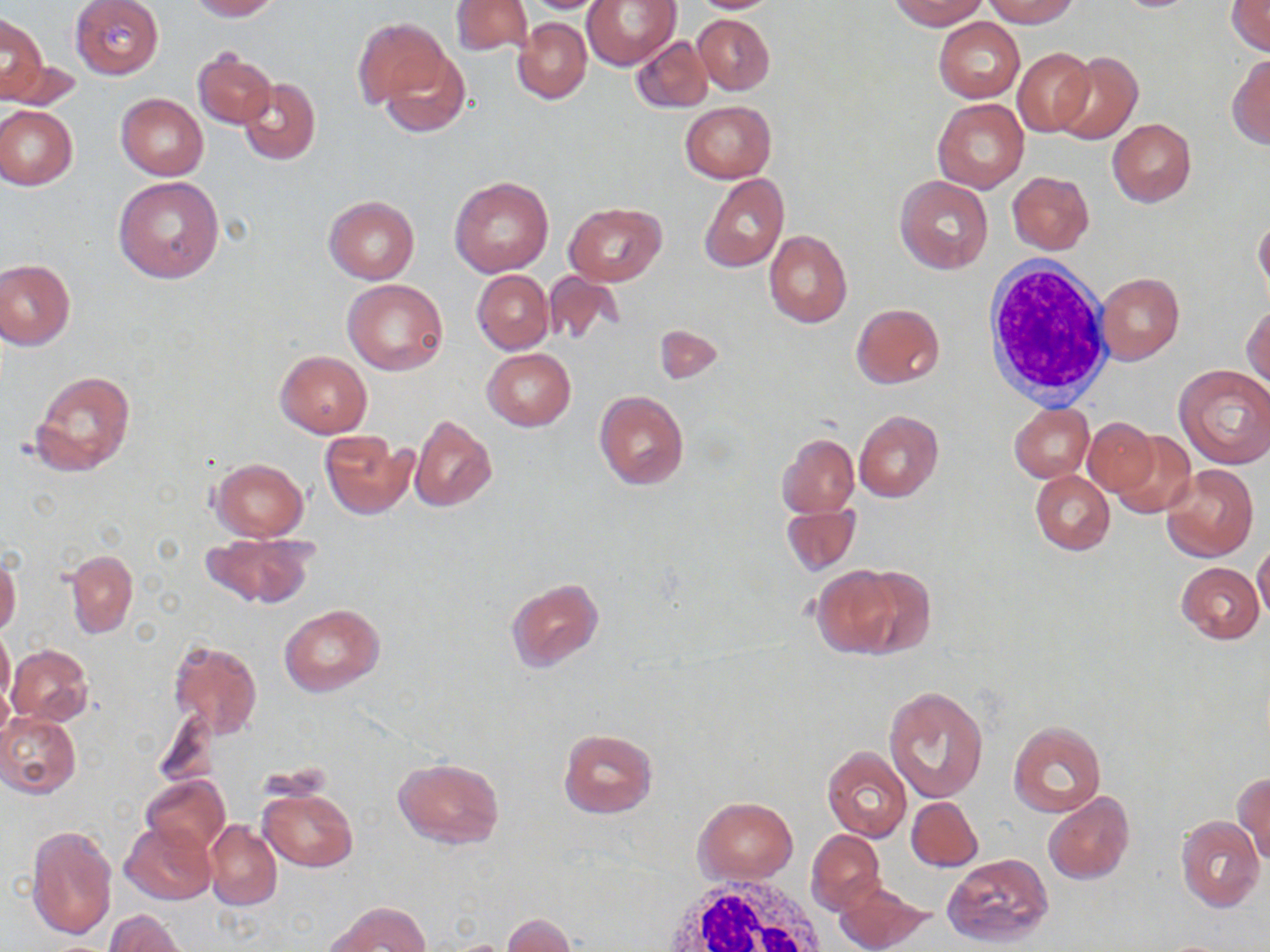
slide-level diagnosis = negative for blood parasites
white blood cell locations = approximate bounding boxes as (x1, y1, x2, y2) in pixels: (981, 258, 1116, 410), (659, 878, 831, 952)
field of view = one of a larger specimen
uninfected red blood cell locations = approximate bounding boxes as (x1, y1, x2, y2) in pixels: (69, 0, 163, 78), (184, 0, 279, 21), (452, 0, 533, 57), (582, 0, 680, 71), (687, 0, 784, 14), (890, 0, 988, 30), (983, 0, 1078, 27), (1227, 0, 1270, 56), (517, 1, 618, 13), (0, 12, 47, 102), (692, 13, 774, 95), (513, 17, 591, 103), (934, 17, 1025, 102), (354, 18, 452, 107), (631, 35, 713, 113), (379, 46, 471, 138), (1013, 47, 1095, 135), (192, 51, 276, 129), (1052, 52, 1142, 143), (1227, 53, 1270, 149), (4, 55, 83, 113), (237, 77, 320, 165), (116, 94, 207, 180), (933, 99, 1028, 193), (681, 100, 775, 183), (0, 106, 77, 190), (1107, 118, 1196, 207), (1007, 171, 1094, 254), (700, 174, 789, 273), (113, 176, 224, 285), (451, 176, 553, 277), (896, 176, 994, 275), (323, 196, 419, 284), (564, 201, 667, 287), (1254, 214, 1270, 303), (764, 231, 853, 328), (0, 259, 75, 351), (472, 270, 553, 354), (542, 271, 627, 347), (1097, 272, 1184, 365), (344, 278, 447, 375), (850, 303, 944, 388), (1244, 305, 1270, 389), (654, 324, 723, 384), (482, 348, 575, 431), (275, 351, 372, 438), (1175, 365, 1270, 469), (28, 368, 137, 478), (594, 390, 689, 489), (1010, 403, 1093, 482), (854, 411, 944, 502), (409, 416, 498, 513), (1085, 417, 1158, 496), (1109, 430, 1197, 519), (319, 431, 417, 519), (777, 432, 859, 518), (210, 458, 309, 541), (1162, 464, 1258, 561), (1030, 469, 1115, 555), (782, 502, 861, 577), (200, 533, 316, 609), (1253, 543, 1270, 623), (66, 549, 138, 638), (0, 554, 21, 637), (1177, 562, 1265, 643), (810, 564, 907, 658), (505, 578, 604, 673), (280, 604, 384, 696), (0, 626, 14, 708), (168, 638, 263, 740), (7, 644, 92, 726), (884, 685, 989, 802), (153, 707, 219, 788), (0, 713, 81, 798), (1008, 720, 1106, 818), (558, 728, 658, 818), (821, 746, 911, 843), (393, 757, 505, 850), (1233, 772, 1270, 861), (140, 774, 230, 854), (259, 787, 357, 871), (1042, 793, 1135, 885), (906, 796, 983, 871), (695, 797, 797, 882), (1175, 816, 1265, 912), (120, 821, 216, 906), (205, 821, 282, 910), (26, 824, 117, 939), (806, 830, 885, 914), (943, 853, 1052, 949), (834, 881, 933, 952), (326, 901, 431, 951), (104, 910, 188, 952), (504, 913, 576, 951)
preparation = thin blood film
modality = optical microscopy
magnification = 1000x
stain = May-Grünwald-Giemsa
image size = 1270×952 pixels